State which cell type is depicted.
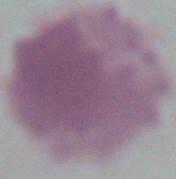
This is an erythrocyte.

magnification = 1000x
modality = photomicrograph